Give the preparation type.
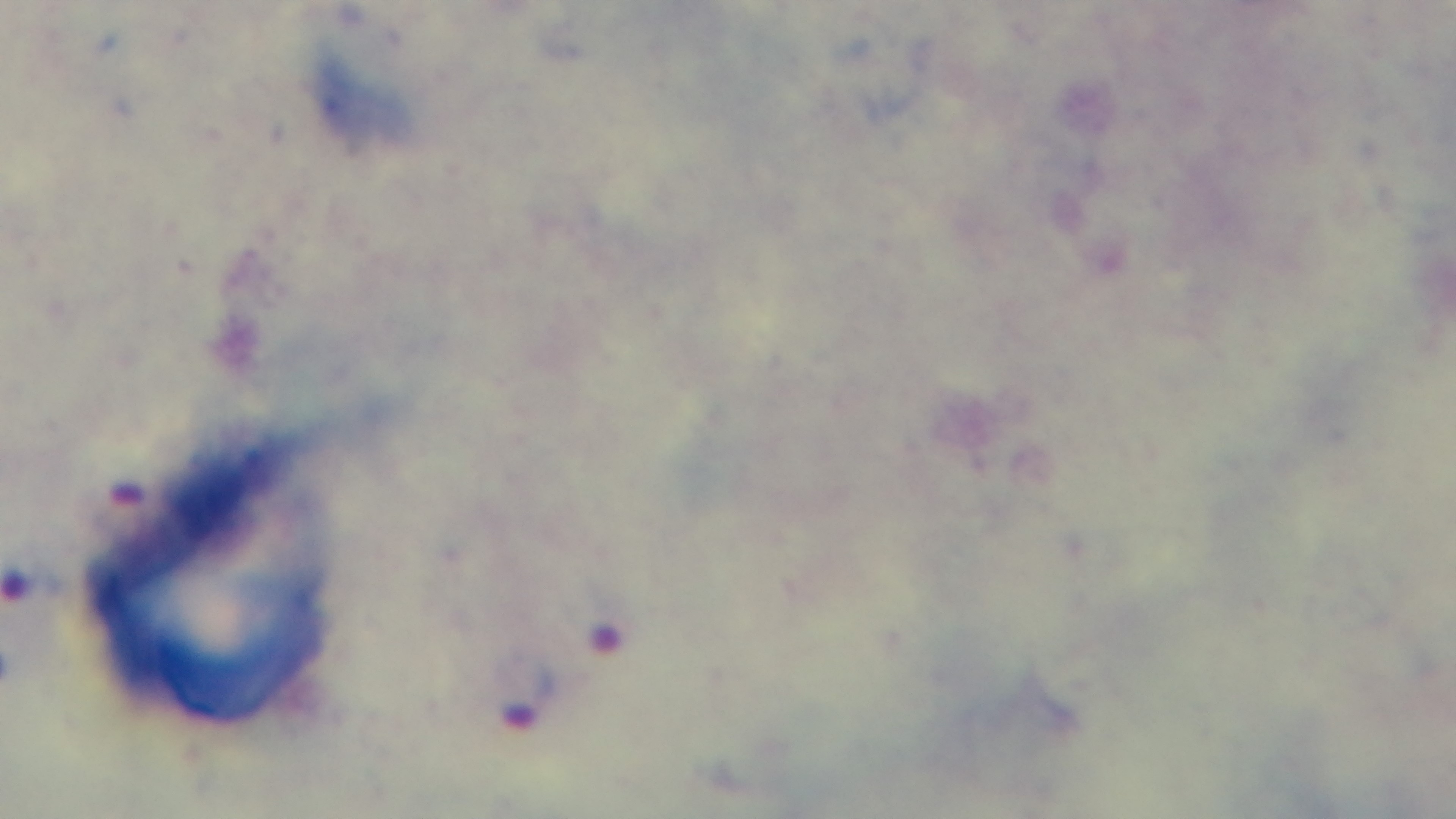
A thick smear.

Summary:
  - Capture: mounted 4K digital camera
  - Field of view: single
  - Modality: light microscopy
  - Objective: 100x oil immersion
  - Stain: Giemsa
  - Malaria status: positive